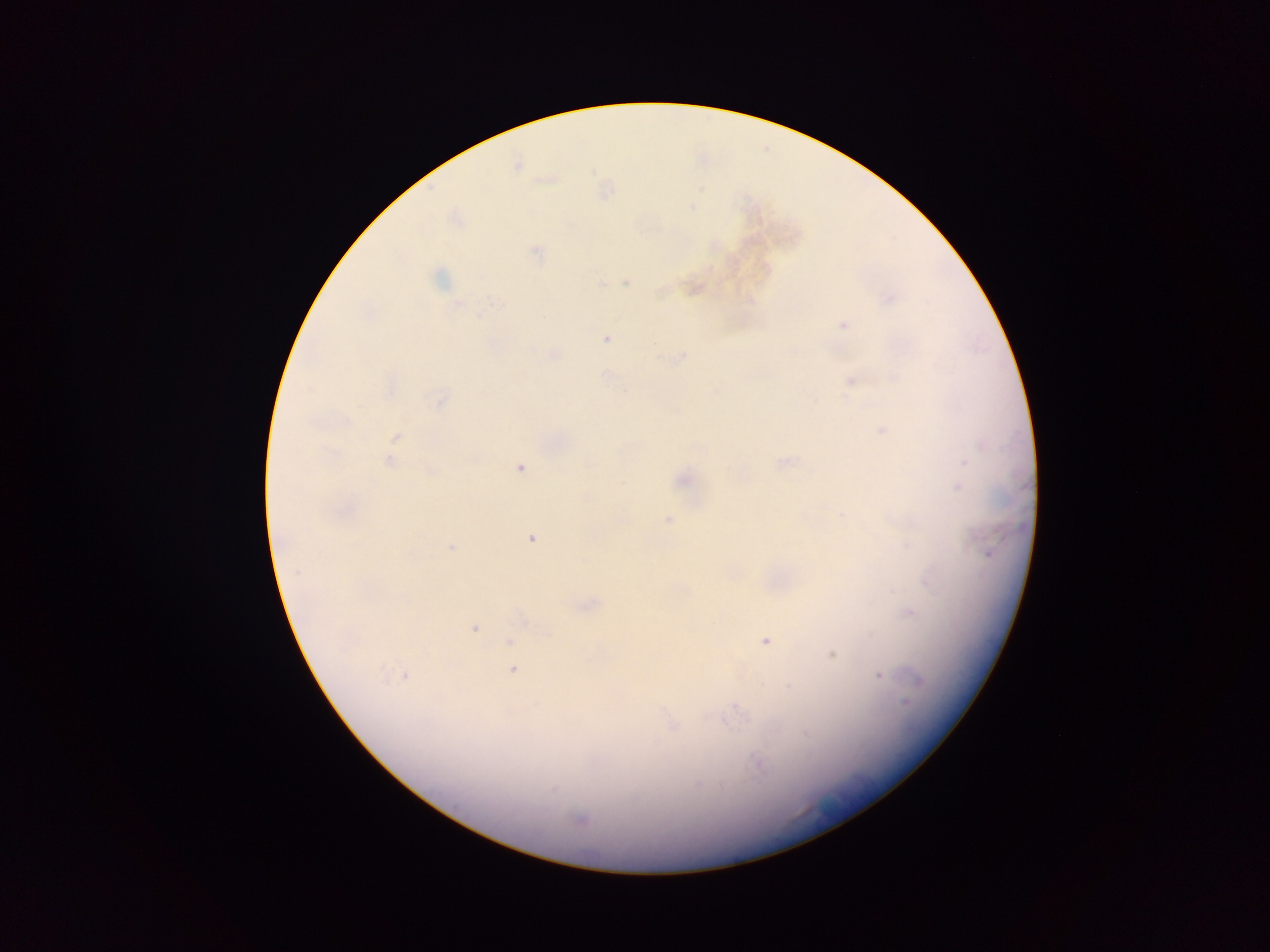
field of view = single
capture = mobile-phone photograph through a microscope
country = Ghana
image size = 1270×952 pixels
Plasmodium parasite locations = approximate centers as {x, y} in pixels: {517, 166}, {692, 207}, {536, 251}, {439, 279}, {601, 283}, {626, 283}, {891, 298}, {494, 303}, {458, 304}, {843, 325}, {606, 339}, {555, 354}, {683, 356}, {851, 381}, {310, 389}, {440, 400}, {346, 421}, {883, 430}, {397, 437}, {334, 453}, {965, 461}, {388, 462}, {520, 468}, {431, 471}, {683, 481}, {958, 488}, {587, 497}, {668, 520}, {531, 539}, {451, 547}, {987, 552}, {297, 572}, {910, 612}, {474, 628}, {765, 641}, {510, 642}, {832, 655}, {513, 670}, {405, 676}, {879, 676}, {918, 680}, {905, 704}, {738, 709}, {673, 725}, {758, 763}, {555, 789}, {580, 819}
preparation = thick blood smear